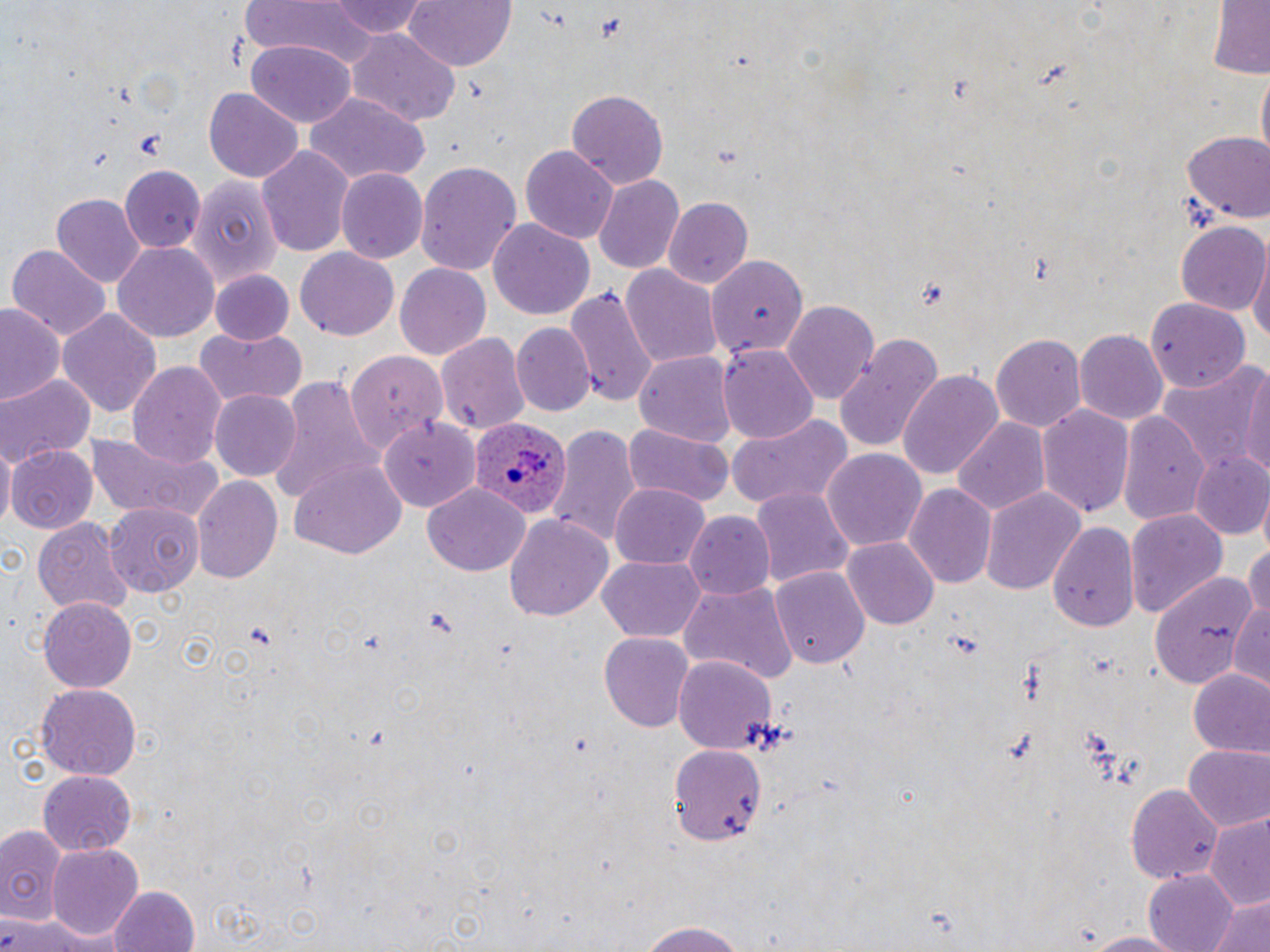

slide-level diagnosis = Plasmodium ovale
magnification = 1000x
uninfected red blood cell locations = approximate bounding boxes as [x1, y1, x2, y2] in pixels: [329, 0, 430, 39], [402, 0, 517, 71], [241, 1, 377, 66], [1203, 2, 1270, 79], [346, 32, 460, 125], [248, 39, 355, 128], [203, 87, 302, 182], [567, 89, 667, 189], [303, 95, 430, 185], [1182, 133, 1269, 223], [257, 144, 355, 261], [519, 144, 619, 243], [416, 161, 522, 280], [121, 165, 205, 254], [337, 168, 430, 263], [187, 172, 280, 312], [594, 173, 685, 273], [53, 194, 144, 286], [662, 196, 754, 290], [489, 218, 596, 320], [1176, 222, 1268, 316], [112, 242, 219, 342], [7, 244, 111, 342], [295, 247, 400, 340], [1249, 247, 1270, 349], [708, 257, 806, 362], [393, 262, 490, 361], [210, 263, 385, 343], [622, 264, 723, 370], [210, 269, 293, 344], [565, 284, 657, 411], [1144, 298, 1250, 393], [784, 299, 881, 404], [0, 301, 66, 409], [59, 309, 161, 418], [512, 323, 595, 417], [194, 329, 309, 412], [1074, 329, 1166, 426], [437, 332, 529, 438], [991, 332, 1086, 434], [834, 333, 946, 452], [718, 345, 818, 445], [343, 351, 442, 452], [635, 351, 738, 447], [1156, 356, 1267, 477], [1241, 357, 1270, 486], [128, 360, 226, 467], [896, 370, 1006, 484], [0, 374, 94, 468], [266, 377, 383, 504], [211, 389, 302, 480], [1036, 402, 1135, 520], [1118, 409, 1211, 525], [726, 411, 855, 515], [953, 416, 1049, 516], [378, 419, 480, 512], [624, 422, 732, 507], [547, 424, 641, 551], [82, 429, 224, 525], [0, 440, 16, 535], [8, 445, 98, 535], [824, 449, 926, 551], [1189, 451, 1270, 540], [288, 458, 405, 559], [191, 475, 282, 586], [610, 481, 711, 567], [423, 482, 529, 576], [902, 483, 995, 591], [751, 486, 854, 591], [981, 486, 1085, 595], [105, 503, 204, 596], [1124, 508, 1228, 620], [684, 512, 775, 599], [504, 513, 615, 622], [33, 517, 132, 616], [1048, 521, 1141, 633], [844, 537, 940, 630], [1243, 543, 1270, 631], [598, 557, 706, 643], [772, 565, 870, 671], [1147, 567, 1261, 688], [675, 578, 798, 685], [1231, 597, 1269, 692], [39, 598, 136, 694], [598, 632, 693, 732], [673, 652, 777, 755], [1186, 668, 1270, 759], [35, 684, 142, 779], [667, 741, 767, 847], [1183, 745, 1270, 831], [36, 771, 136, 854], [1126, 781, 1224, 888], [1205, 817, 1270, 913], [0, 823, 65, 925], [46, 843, 144, 938], [4, 859, 77, 945], [1143, 869, 1241, 952], [107, 885, 200, 952], [1205, 894, 1270, 952], [0, 914, 87, 952], [634, 923, 752, 952], [1073, 930, 1191, 951]
stain = May-Grünwald-Giemsa
Plasmodium ovale-infected red blood cell locations = approximate bounding boxes as [x1, y1, x2, y2] in pixels: [467, 417, 573, 518]
image size = 1270×952 pixels
modality = light microscopy
preparation = thin blood film
field of view = single